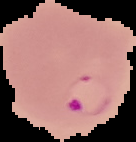
image size = 136×142 pixels
result = malaria parasites detected
preparation = thin blood smear
image type = cell region segmented out of the field of view; surrounding area masked to black